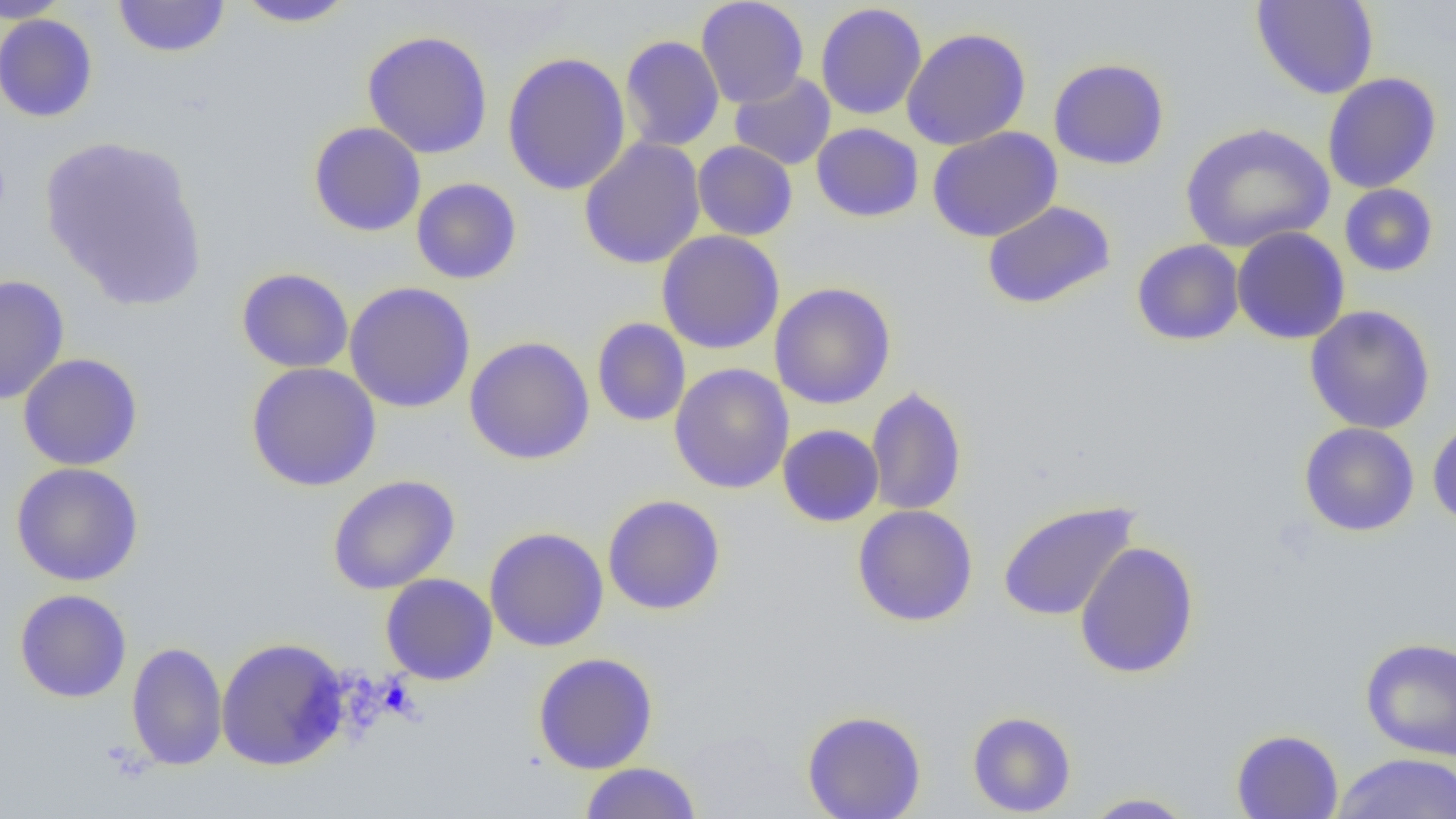
Summary:
  - Coordinate format: approximate bounding boxes as [x1, y1, x2, y2] in pixels
  - Uninfected red blood cell locations: [113, 0, 229, 57], [234, 0, 357, 28], [696, 0, 809, 108], [1250, 0, 1380, 100], [0, 1, 74, 23], [815, 3, 927, 120], [0, 13, 99, 123], [901, 27, 1031, 150], [362, 30, 494, 159], [619, 34, 725, 152], [502, 51, 631, 196], [1048, 58, 1169, 170], [729, 72, 836, 170], [1322, 72, 1441, 193], [308, 121, 426, 237], [811, 123, 924, 222], [1181, 123, 1334, 252], [927, 126, 1063, 242], [39, 135, 208, 310], [578, 137, 706, 270], [693, 141, 798, 241], [411, 178, 522, 284], [1339, 184, 1439, 277], [982, 200, 1116, 310], [1231, 226, 1350, 344], [656, 230, 785, 354], [1131, 239, 1245, 346], [236, 267, 354, 373], [0, 274, 70, 406], [343, 281, 476, 413], [769, 282, 896, 409], [1304, 305, 1436, 434], [592, 317, 691, 427], [464, 336, 595, 465], [18, 353, 143, 471], [246, 362, 382, 492], [669, 363, 794, 494], [865, 386, 967, 516], [1427, 417, 1456, 529], [1299, 422, 1420, 537], [777, 424, 884, 527], [11, 462, 144, 586], [327, 475, 460, 594], [602, 494, 726, 615], [997, 500, 1140, 622], [851, 504, 979, 627], [484, 527, 609, 652], [1074, 541, 1200, 679], [380, 573, 498, 685], [14, 589, 132, 703], [215, 637, 350, 771], [1360, 637, 1456, 760], [126, 642, 228, 771], [533, 652, 659, 774], [801, 709, 927, 819], [967, 710, 1077, 817], [1230, 729, 1343, 819], [1331, 752, 1456, 819], [579, 762, 703, 818], [1080, 792, 1198, 818]
  - Slide-level diagnosis: no evidence of blood parasites
  - Image size: 1456×819 pixels
  - Magnification: 1000x
  - Modality: light microscopy
  - Preparation: thin blood smear
  - Field of view: one of a larger specimen